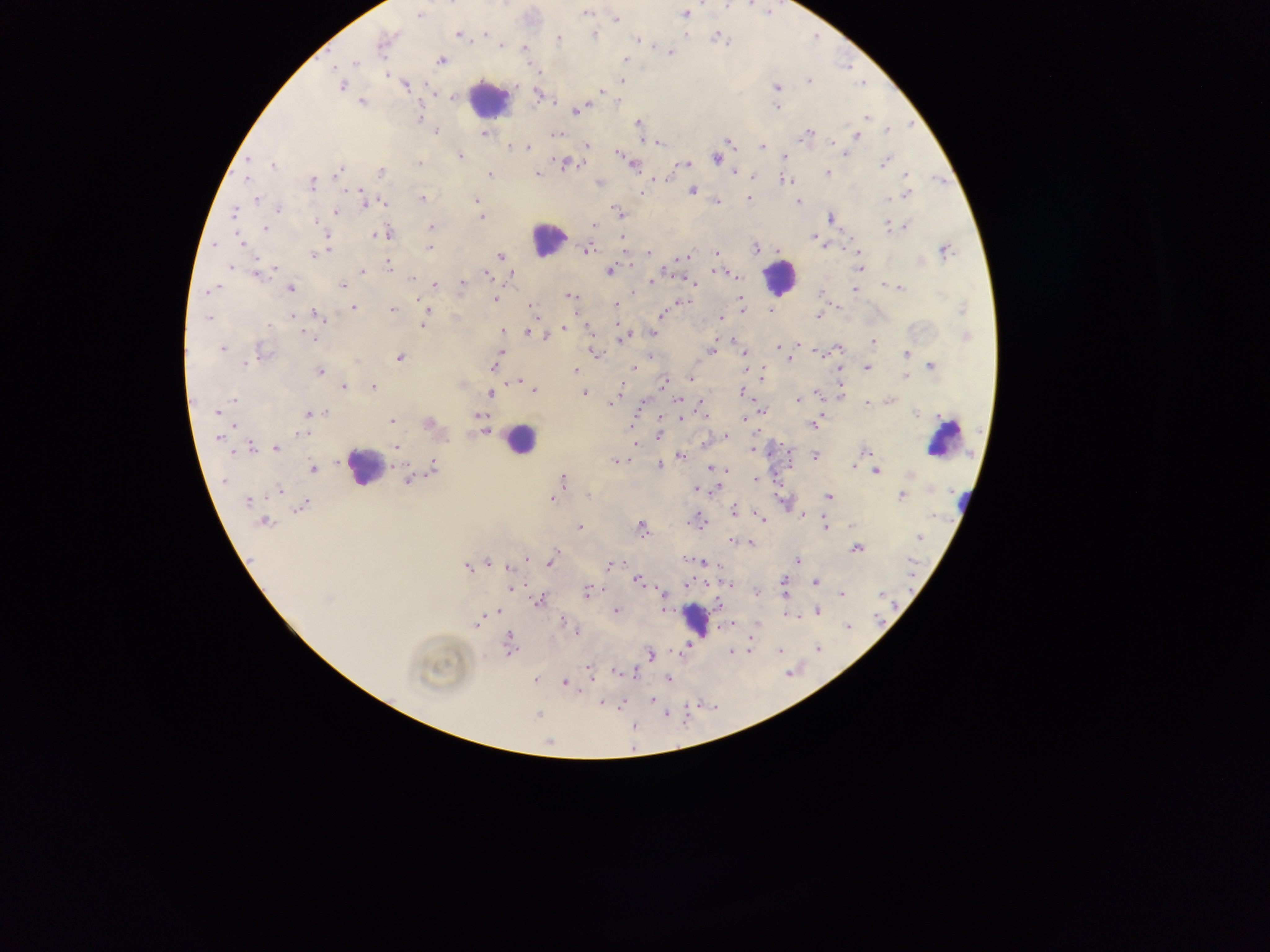

Approximate centers as (x, y) in pixels.
Summary:
  - Malaria parasite locations: (587, 12), (685, 14), (420, 15), (616, 19), (458, 34), (485, 34), (595, 35), (715, 37), (558, 39), (636, 40), (381, 44), (502, 46), (524, 49), (670, 52), (441, 60), (625, 61), (354, 62), (537, 70), (387, 75), (622, 81), (809, 81), (406, 85), (341, 86), (777, 88), (601, 91), (538, 95), (453, 98), (362, 102), (777, 108), (578, 110), (419, 117), (868, 117), (638, 123), (435, 130), (887, 130), (483, 133), (806, 133), (556, 134), (857, 136), (726, 142), (832, 142), (660, 143), (587, 145), (762, 145), (510, 146), (528, 148), (618, 154), (846, 154), (460, 156), (785, 156), (717, 158), (249, 160), (885, 162), (419, 164), (565, 164), (685, 164), (273, 165), (634, 165), (339, 172), (380, 172), (736, 172), (827, 173), (489, 174), (537, 174), (907, 175), (751, 176), (247, 178), (785, 179), (599, 183), (312, 184), (692, 191), (361, 192), (643, 192), (908, 193), (422, 198), (749, 198), (476, 199), (889, 199), (257, 200), (365, 200), (797, 202), (383, 203), (717, 203), (369, 204), (278, 209), (234, 212), (335, 212), (618, 212), (481, 216), (830, 217), (315, 222), (595, 225), (889, 226), (431, 227), (905, 227), (264, 228), (381, 235), (328, 236), (815, 238), (240, 241), (823, 245), (327, 246), (430, 248), (756, 249), (588, 250), (858, 250), (649, 252), (945, 252), (715, 253), (314, 254), (500, 256), (683, 258), (388, 266), (232, 267), (275, 268), (858, 268), (271, 271), (610, 271), (362, 272), (259, 274), (486, 274), (511, 274), (734, 276), (412, 278), (652, 280), (435, 284), (462, 284), (883, 284), (343, 285), (213, 288), (291, 288), (900, 288), (854, 289), (821, 293), (570, 295), (494, 300), (741, 301), (684, 302), (615, 305), (353, 307), (531, 307), (743, 308), (392, 309), (963, 309), (428, 310), (771, 311), (662, 315), (292, 316), (317, 316), (819, 316), (721, 317), (208, 318), (423, 324), (268, 326), (564, 328), (589, 329), (502, 331), (530, 332), (652, 334), (544, 336), (966, 336), (313, 338), (622, 338), (873, 341), (798, 345), (778, 347), (837, 349), (222, 350), (711, 350), (501, 351), (262, 352), (595, 353), (744, 353), (906, 353), (399, 358), (650, 358), (789, 359), (496, 361), (246, 364), (932, 366), (493, 367), (635, 367), (868, 367), (320, 371), (574, 371), (763, 375), (906, 377), (691, 378), (518, 382), (664, 382), (343, 387), (373, 387), (621, 388), (841, 389), (534, 390), (742, 392), (491, 393), (584, 394), (819, 394), (799, 399), (234, 400), (889, 400), (701, 401), (612, 402), (868, 403), (679, 411), (217, 412), (763, 412), (310, 413), (324, 413), (916, 413), (479, 416), (681, 418), (744, 419), (392, 420), (429, 423), (813, 424), (483, 431), (301, 434), (659, 435), (726, 436), (218, 438), (396, 447), (250, 448), (257, 448), (276, 448), (753, 449), (866, 452), (681, 456), (815, 456), (616, 461), (661, 465), (854, 465), (313, 468), (714, 468), (433, 469), (877, 472), (909, 474), (757, 479), (407, 480), (562, 480), (223, 481), (696, 490), (279, 492), (828, 496), (902, 496), (552, 498), (247, 502), (304, 505), (733, 511), (762, 519), (696, 521), (265, 523), (853, 526), (580, 527), (641, 527), (825, 527), (919, 538), (732, 541), (750, 543), (857, 548), (526, 559), (797, 559), (551, 561), (701, 562), (488, 563), (611, 564), (467, 567), (510, 567), (637, 580), (783, 581), (816, 583), (728, 585), (512, 587), (785, 589), (587, 592), (756, 592), (663, 594), (842, 595), (327, 600), (539, 601), (617, 611), (817, 611), (496, 612), (476, 623), (564, 623), (758, 625), (848, 627), (572, 630), (575, 632), (508, 642), (817, 648), (749, 650), (731, 651), (779, 651), (650, 655), (588, 668), (616, 672), (634, 674), (668, 679), (535, 680), (564, 683), (653, 700), (602, 703)
  - Leukocyte locations: (488, 98), (547, 239), (779, 278), (942, 438), (520, 440), (364, 466), (962, 497), (696, 619)
  - Capture: mobile-phone photograph through a microscope
  - Image size: 1270×952 pixels
  - Field of view: single
  - Country: Ghana
  - Preparation: thick blood smear